State which parasite is depicted.
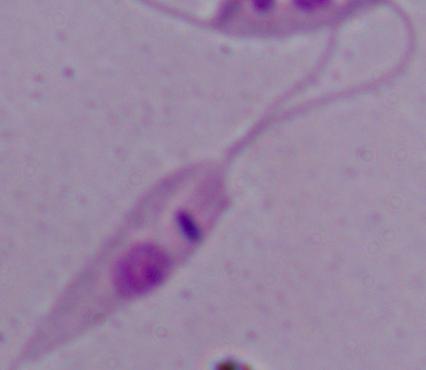
This is Leishmania.

1000x magnification. Micrograph.